Identify the parasite.
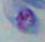
Toxoplasma gondii.

modality: micrograph
magnification: 1000x